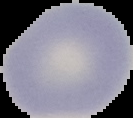
Malaria status: uninfected. Cell region segmented out of the field of view; the surrounding area is masked to black. From a thin blood film. Image is 133×118 pixels.